Name the blood parasite species.
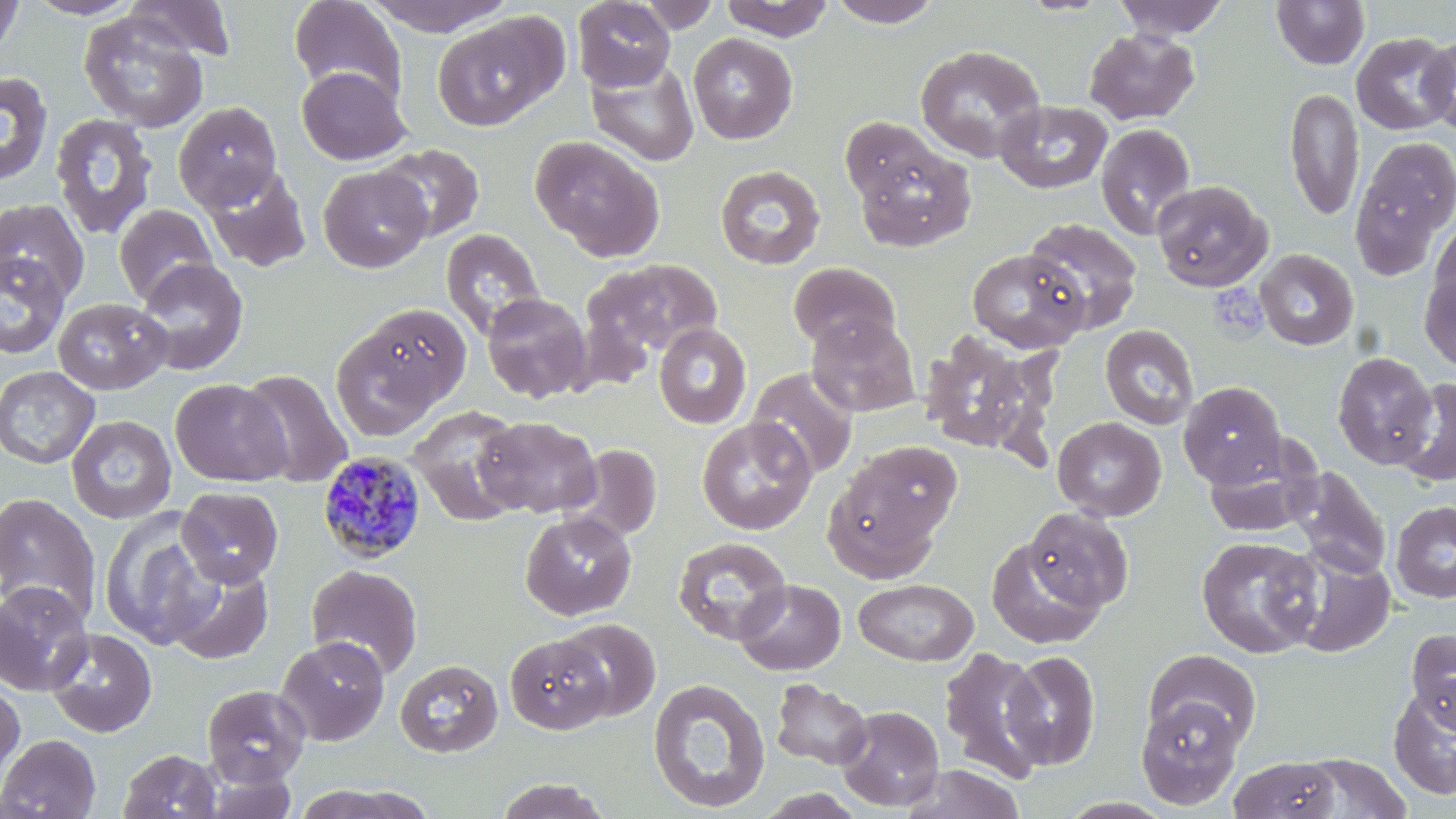
Plasmodium malariae.

Summary:
  - Coordinate format: approximate bounding boxes as (x1, y1, x2, y2) in pixels
  - Plasmodium malariae-infected red blood cell locations: (317, 451, 426, 565)
  - Uninfected red blood cell locations: (0, 0, 24, 60), (22, 0, 142, 20), (125, 0, 239, 61), (288, 0, 407, 102), (362, 0, 519, 36), (572, 0, 675, 90), (719, 0, 836, 41), (826, 0, 945, 27), (1111, 0, 1230, 40), (1271, 0, 1370, 69), (633, 1, 720, 31), (79, 12, 210, 133), (432, 13, 566, 132), (1083, 28, 1200, 125), (1352, 32, 1455, 135), (688, 33, 797, 144), (1418, 33, 1454, 134), (915, 45, 1046, 163), (586, 58, 698, 166), (296, 66, 411, 165), (0, 71, 53, 186), (1284, 85, 1364, 222), (173, 100, 283, 211), (995, 100, 1112, 194), (49, 113, 159, 240), (1095, 123, 1196, 240), (847, 131, 976, 252), (529, 134, 666, 262), (1349, 136, 1456, 280), (376, 144, 485, 243), (715, 164, 826, 270), (202, 165, 311, 273), (318, 165, 432, 272), (1151, 180, 1273, 293), (0, 199, 90, 304), (113, 204, 218, 307), (1022, 217, 1143, 333), (1427, 217, 1456, 318), (441, 228, 547, 340), (967, 248, 1089, 353), (1254, 248, 1359, 350), (0, 253, 70, 360), (134, 258, 249, 376), (590, 258, 723, 358), (788, 261, 901, 354), (1420, 266, 1456, 374), (482, 293, 592, 403), (53, 298, 172, 394), (333, 307, 466, 435), (805, 314, 920, 417), (653, 323, 752, 429), (1100, 324, 1199, 430), (918, 330, 1060, 459), (1333, 352, 1436, 470), (0, 366, 100, 469), (747, 368, 859, 480), (238, 369, 354, 487), (1392, 378, 1456, 486), (170, 379, 290, 486), (1179, 381, 1286, 487), (408, 406, 526, 526), (66, 415, 177, 524), (476, 415, 602, 518), (1052, 416, 1166, 521), (697, 417, 817, 535), (1203, 439, 1323, 537), (848, 442, 962, 543), (565, 443, 662, 542), (821, 465, 946, 582), (1289, 469, 1390, 578), (176, 487, 284, 588), (0, 492, 102, 622), (1391, 501, 1456, 603), (99, 507, 221, 652), (1024, 507, 1133, 613), (520, 511, 637, 621), (1197, 535, 1323, 658), (673, 537, 792, 644), (986, 538, 1102, 649), (1288, 551, 1395, 658), (165, 563, 275, 664), (306, 564, 423, 679), (853, 578, 979, 666), (735, 579, 846, 676), (0, 582, 93, 696), (556, 618, 661, 721), (1406, 627, 1456, 729), (45, 628, 157, 737), (505, 633, 611, 734), (276, 636, 390, 745), (938, 646, 1051, 783), (1144, 649, 1263, 750), (1003, 650, 1101, 770), (395, 659, 503, 757), (0, 676, 25, 783), (648, 677, 771, 813), (770, 678, 874, 771), (1388, 683, 1456, 800), (201, 684, 311, 787), (1135, 698, 1244, 809), (834, 704, 945, 811), (0, 734, 101, 818), (118, 749, 221, 819), (1301, 752, 1411, 818), (1229, 755, 1343, 819), (898, 765, 1027, 819), (198, 767, 298, 819), (493, 778, 613, 818), (296, 785, 438, 819), (756, 788, 871, 819)
  - Platelet locations: (1207, 290, 1262, 341)
  - Modality: optical microscopy
  - Image size: 1456×819 pixels
  - Stain: May-Grünwald-Giemsa
  - Preparation: thin blood film
  - Magnification: 1000x
  - Field of view: one of a larger specimen